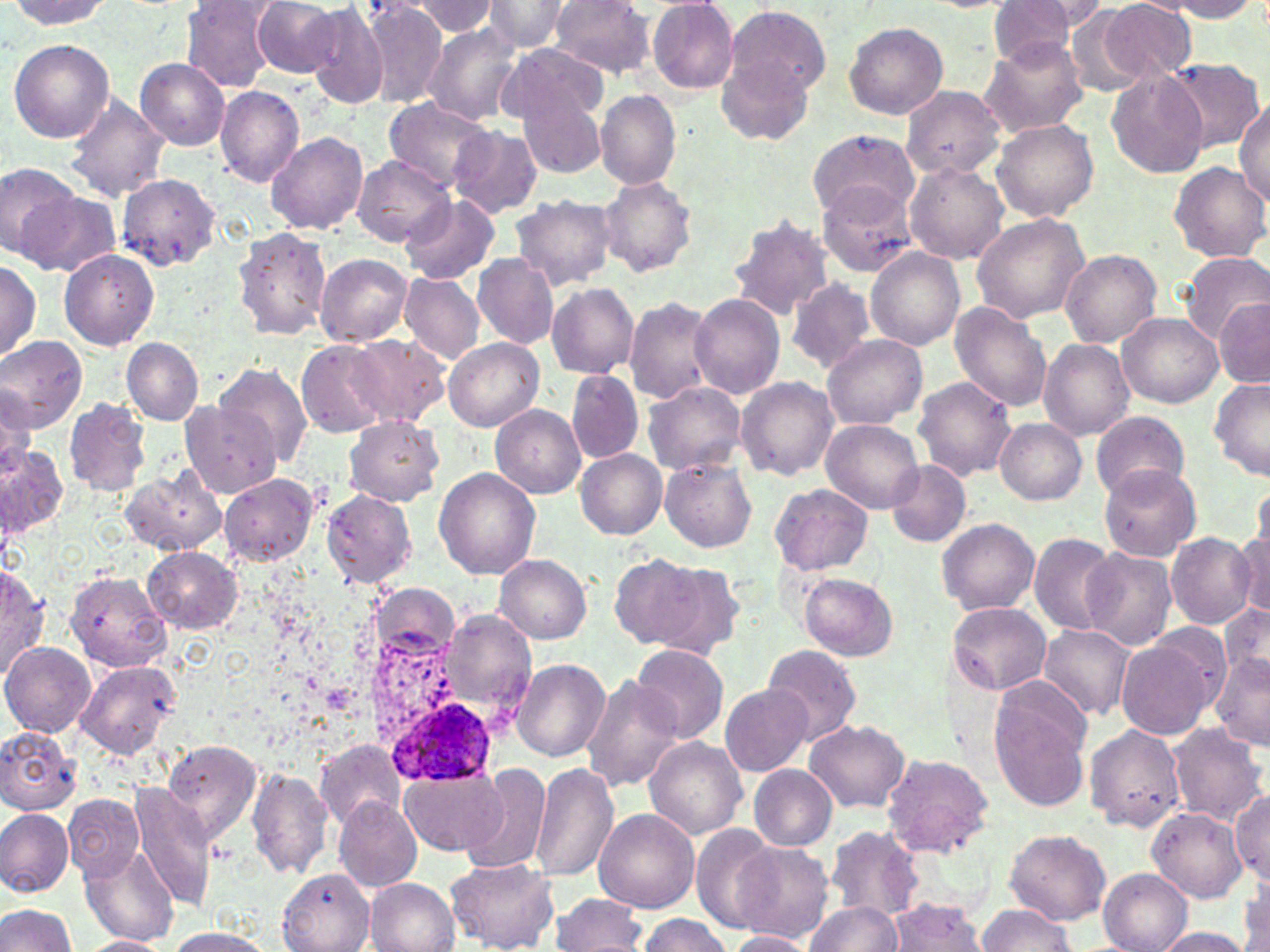
Approximate bounding boxes as named x1/y1/x2/y2 corners in pixels. Uninfected red blood cell locations: (x1=253, y1=0, x2=343, y2=78), (x1=362, y1=0, x2=447, y2=107), (x1=481, y1=0, x2=570, y2=54), (x1=548, y1=0, x2=654, y2=76), (x1=647, y1=0, x2=739, y2=94), (x1=1165, y1=0, x2=1263, y2=21), (x1=8, y1=1, x2=112, y2=29), (x1=408, y1=1, x2=501, y2=36), (x1=1005, y1=1, x2=1107, y2=41), (x1=184, y1=2, x2=281, y2=91), (x1=1096, y1=2, x2=1195, y2=82), (x1=983, y1=3, x2=1084, y2=67), (x1=724, y1=4, x2=828, y2=104), (x1=306, y1=5, x2=389, y2=108), (x1=1065, y1=10, x2=1146, y2=94), (x1=844, y1=22, x2=948, y2=119), (x1=421, y1=23, x2=522, y2=124), (x1=977, y1=38, x2=1088, y2=138), (x1=8, y1=39, x2=114, y2=144), (x1=499, y1=43, x2=607, y2=125), (x1=715, y1=53, x2=814, y2=150), (x1=137, y1=58, x2=229, y2=148), (x1=1164, y1=58, x2=1264, y2=153), (x1=1106, y1=67, x2=1208, y2=178), (x1=898, y1=84, x2=1008, y2=181), (x1=215, y1=86, x2=305, y2=186), (x1=596, y1=89, x2=681, y2=188), (x1=519, y1=90, x2=608, y2=180), (x1=64, y1=93, x2=171, y2=202), (x1=383, y1=96, x2=493, y2=192), (x1=1234, y1=100, x2=1270, y2=207), (x1=991, y1=118, x2=1099, y2=221), (x1=449, y1=125, x2=542, y2=217), (x1=806, y1=128, x2=919, y2=219), (x1=264, y1=132, x2=368, y2=234), (x1=351, y1=156, x2=453, y2=245), (x1=1168, y1=161, x2=1268, y2=264), (x1=905, y1=162, x2=1009, y2=264), (x1=1, y1=164, x2=79, y2=258), (x1=116, y1=175, x2=220, y2=269), (x1=597, y1=176, x2=696, y2=278), (x1=817, y1=182, x2=919, y2=275), (x1=16, y1=191, x2=119, y2=278), (x1=511, y1=193, x2=616, y2=290), (x1=400, y1=195, x2=500, y2=284), (x1=970, y1=211, x2=1090, y2=323), (x1=727, y1=215, x2=834, y2=319), (x1=232, y1=227, x2=332, y2=340), (x1=866, y1=247, x2=965, y2=349), (x1=1059, y1=249, x2=1162, y2=347), (x1=60, y1=250, x2=158, y2=349), (x1=1179, y1=251, x2=1270, y2=341), (x1=472, y1=252, x2=559, y2=350), (x1=315, y1=253, x2=412, y2=346), (x1=0, y1=259, x2=41, y2=360), (x1=400, y1=272, x2=483, y2=364), (x1=786, y1=278, x2=877, y2=374), (x1=547, y1=282, x2=638, y2=378), (x1=690, y1=293, x2=785, y2=399), (x1=624, y1=296, x2=717, y2=403), (x1=1217, y1=298, x2=1269, y2=385), (x1=950, y1=302, x2=1054, y2=410), (x1=1118, y1=311, x2=1223, y2=407), (x1=345, y1=335, x2=450, y2=426), (x1=822, y1=335, x2=926, y2=429), (x1=0, y1=336, x2=87, y2=432), (x1=123, y1=337, x2=204, y2=424), (x1=444, y1=337, x2=544, y2=431), (x1=296, y1=340, x2=389, y2=437), (x1=1039, y1=340, x2=1134, y2=438), (x1=214, y1=363, x2=313, y2=466), (x1=566, y1=370, x2=643, y2=464), (x1=737, y1=377, x2=838, y2=481), (x1=912, y1=377, x2=1017, y2=481), (x1=1209, y1=378, x2=1270, y2=482), (x1=642, y1=381, x2=745, y2=475), (x1=1, y1=387, x2=34, y2=486), (x1=63, y1=397, x2=151, y2=497), (x1=182, y1=401, x2=281, y2=495), (x1=490, y1=404, x2=586, y2=498), (x1=1091, y1=410, x2=1189, y2=500), (x1=345, y1=417, x2=442, y2=506), (x1=821, y1=419, x2=925, y2=514), (x1=995, y1=419, x2=1086, y2=504), (x1=1, y1=444, x2=69, y2=538), (x1=576, y1=450, x2=666, y2=539), (x1=660, y1=457, x2=757, y2=551), (x1=885, y1=460, x2=972, y2=548), (x1=1099, y1=464, x2=1201, y2=561), (x1=433, y1=467, x2=539, y2=580), (x1=120, y1=469, x2=225, y2=557), (x1=220, y1=473, x2=318, y2=566), (x1=770, y1=483, x2=872, y2=576), (x1=1252, y1=483, x2=1269, y2=558), (x1=322, y1=490, x2=416, y2=585), (x1=937, y1=518, x2=1039, y2=614), (x1=1231, y1=530, x2=1269, y2=619), (x1=1166, y1=532, x2=1258, y2=628), (x1=1028, y1=533, x2=1118, y2=634), (x1=145, y1=547, x2=241, y2=632), (x1=1081, y1=548, x2=1177, y2=650), (x1=495, y1=554, x2=592, y2=643), (x1=610, y1=554, x2=711, y2=648), (x1=643, y1=560, x2=746, y2=658), (x1=0, y1=564, x2=49, y2=682), (x1=65, y1=571, x2=171, y2=671), (x1=800, y1=573, x2=897, y2=661), (x1=946, y1=601, x2=1051, y2=696), (x1=1219, y1=602, x2=1269, y2=687), (x1=442, y1=609, x2=535, y2=712), (x1=1039, y1=624, x2=1134, y2=720), (x1=1118, y1=639, x2=1218, y2=740), (x1=1, y1=640, x2=96, y2=737), (x1=631, y1=643, x2=729, y2=745), (x1=762, y1=645, x2=861, y2=745), (x1=1212, y1=653, x2=1270, y2=752), (x1=512, y1=658, x2=610, y2=762), (x1=74, y1=660, x2=181, y2=758), (x1=581, y1=675, x2=683, y2=793), (x1=721, y1=684, x2=812, y2=776), (x1=991, y1=696, x2=1091, y2=811), (x1=805, y1=720, x2=910, y2=813), (x1=1084, y1=722, x2=1186, y2=833), (x1=1166, y1=723, x2=1267, y2=828), (x1=0, y1=726, x2=80, y2=815), (x1=644, y1=736, x2=747, y2=838), (x1=314, y1=739, x2=406, y2=832), (x1=164, y1=740, x2=262, y2=847), (x1=881, y1=753, x2=994, y2=857), (x1=531, y1=763, x2=619, y2=884), (x1=749, y1=765, x2=837, y2=851), (x1=463, y1=766, x2=551, y2=877), (x1=246, y1=768, x2=335, y2=880), (x1=398, y1=769, x2=508, y2=856), (x1=131, y1=784, x2=215, y2=908), (x1=1230, y1=792, x2=1269, y2=887), (x1=64, y1=794, x2=144, y2=881), (x1=335, y1=798, x2=421, y2=891), (x1=0, y1=808, x2=73, y2=896), (x1=1147, y1=809, x2=1247, y2=902), (x1=594, y1=810, x2=699, y2=912), (x1=690, y1=824, x2=781, y2=932), (x1=825, y1=825, x2=925, y2=922), (x1=1004, y1=829, x2=1112, y2=925), (x1=733, y1=842, x2=833, y2=941), (x1=82, y1=844, x2=178, y2=946), (x1=444, y1=856, x2=559, y2=952), (x1=279, y1=869, x2=377, y2=951), (x1=1099, y1=869, x2=1192, y2=952), (x1=1240, y1=874, x2=1269, y2=952), (x1=364, y1=878, x2=458, y2=952), (x1=551, y1=893, x2=647, y2=951), (x1=884, y1=899, x2=987, y2=951), (x1=805, y1=900, x2=901, y2=952), (x1=0, y1=903, x2=77, y2=952), (x1=975, y1=903, x2=1075, y2=952), (x1=634, y1=914, x2=732, y2=951), (x1=1150, y1=927, x2=1254, y2=951), (x1=163, y1=928, x2=278, y2=951), (x1=724, y1=929, x2=815, y2=951), (x1=71, y1=935, x2=173, y2=951). Plasmodium ovale-infected red blood cell locations: (x1=389, y1=698, x2=492, y2=784). Slide-level diagnosis: Plasmodium ovale. Thin blood smear. Captured at 1000x magnification. Single field of view. May-Grünwald-Giemsa stain. Light microscopy. Image is 1270×952 pixels.